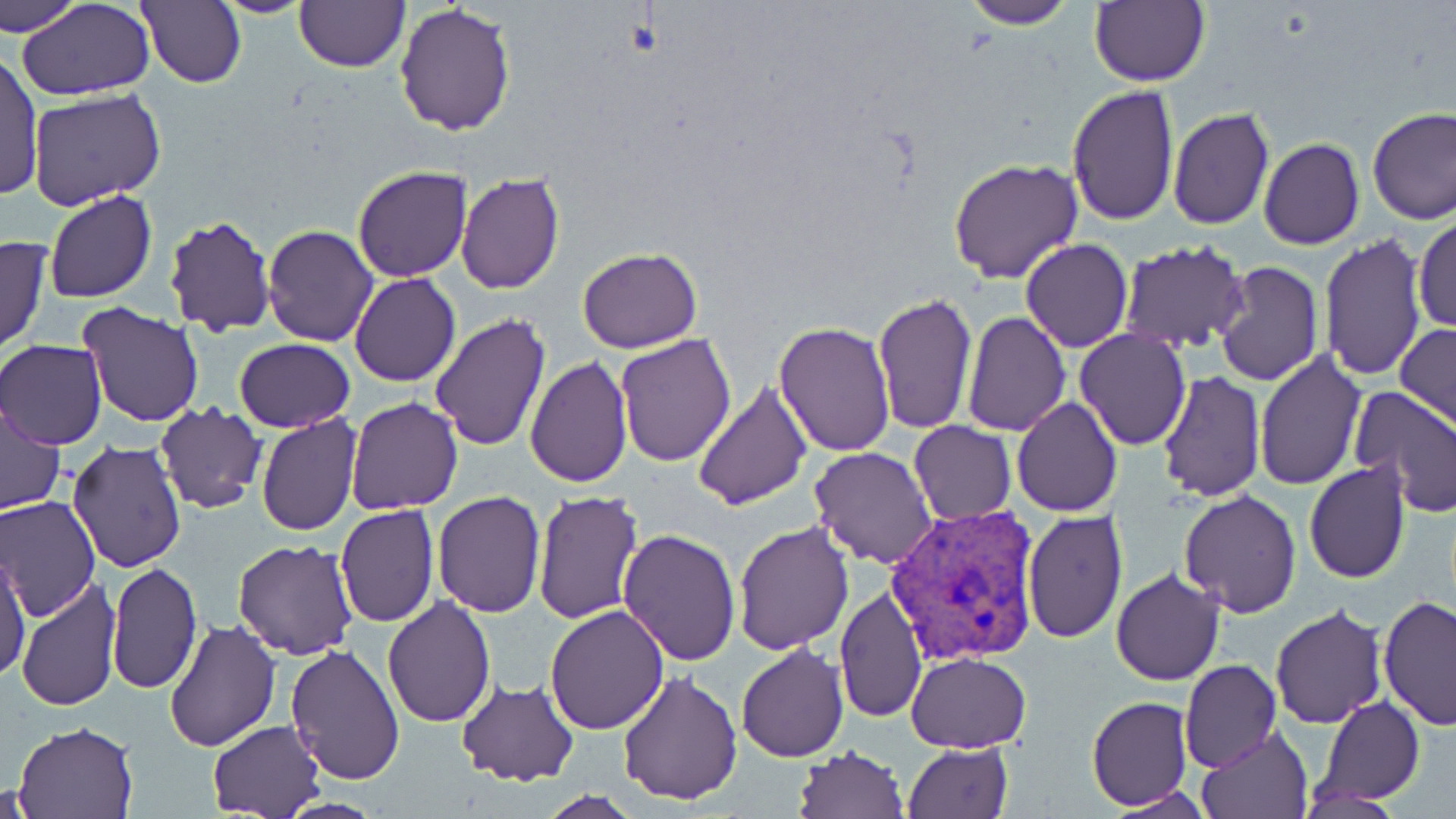

Plasmodium vivax-infected red blood cell locations = approximate bounding boxes as (x1, y1, x2, y2) in pixels: (889, 503, 1040, 664)
slide-level diagnosis = Plasmodium vivax
field of view = one of a larger specimen
magnification = 1000x
image size = 1456×819 pixels
uninfected red blood cell locations = approximate bounding boxes as (x1, y1, x2, y2) in pixels: (1, 0, 85, 37), (18, 0, 154, 100), (139, 0, 246, 89), (212, 0, 317, 17), (961, 0, 1074, 27), (1088, 1, 1210, 87), (294, 2, 408, 71), (395, 2, 518, 138), (1, 49, 44, 203), (1065, 85, 1179, 228), (27, 87, 167, 209), (1167, 106, 1275, 231), (1366, 106, 1456, 225), (1258, 137, 1365, 249), (948, 158, 1082, 284), (352, 165, 471, 281), (456, 170, 567, 293), (44, 190, 157, 304), (164, 212, 277, 337), (1413, 215, 1455, 333), (262, 225, 380, 347), (0, 234, 52, 355), (1319, 234, 1427, 381), (1020, 238, 1133, 352), (1118, 241, 1251, 352), (577, 247, 702, 353), (1214, 261, 1323, 387), (351, 273, 461, 387), (871, 292, 977, 435), (77, 302, 203, 427), (960, 310, 1070, 434), (429, 312, 552, 452), (773, 319, 895, 456), (1396, 322, 1456, 431), (1076, 329, 1190, 449), (615, 333, 738, 467), (233, 338, 357, 433), (0, 340, 106, 450), (1254, 349, 1366, 492), (524, 354, 632, 489), (1156, 371, 1266, 502), (693, 380, 813, 511), (1350, 386, 1456, 516), (346, 397, 463, 514), (1011, 398, 1122, 517), (155, 401, 268, 516), (0, 403, 66, 516), (256, 415, 361, 537), (909, 420, 1016, 526), (66, 440, 188, 576), (809, 447, 937, 568), (1303, 462, 1411, 584), (1177, 488, 1301, 619), (532, 490, 644, 624), (432, 492, 545, 617), (1, 496, 100, 620), (334, 505, 440, 627), (1021, 510, 1129, 646), (733, 520, 855, 654), (617, 529, 742, 666), (233, 540, 361, 660), (0, 547, 31, 684), (108, 563, 202, 694), (1109, 568, 1224, 687), (16, 578, 122, 712), (833, 586, 928, 722), (383, 594, 496, 724), (1378, 594, 1456, 730), (1270, 604, 1387, 728), (546, 606, 669, 734), (164, 619, 282, 753), (284, 643, 407, 785), (736, 643, 849, 763), (907, 653, 1030, 753), (1179, 659, 1283, 771), (618, 672, 742, 805), (456, 680, 580, 784), (1087, 696, 1194, 809), (1317, 696, 1423, 805), (207, 720, 327, 818), (11, 721, 140, 818), (1197, 727, 1313, 818), (903, 742, 1013, 819), (795, 746, 908, 819), (2, 779, 42, 818), (533, 792, 644, 819)
stain = May-Grünwald-Giemsa
preparation = thin blood film
modality = optical microscopy